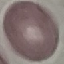
malaria status = uninfected
image type = automatically extracted cell patch, resized to 64 × 64 pixels
preparation = thin smear
capture = smartphone through the microscope eyepiece
stain = Giemsa